Identify the preparation type.
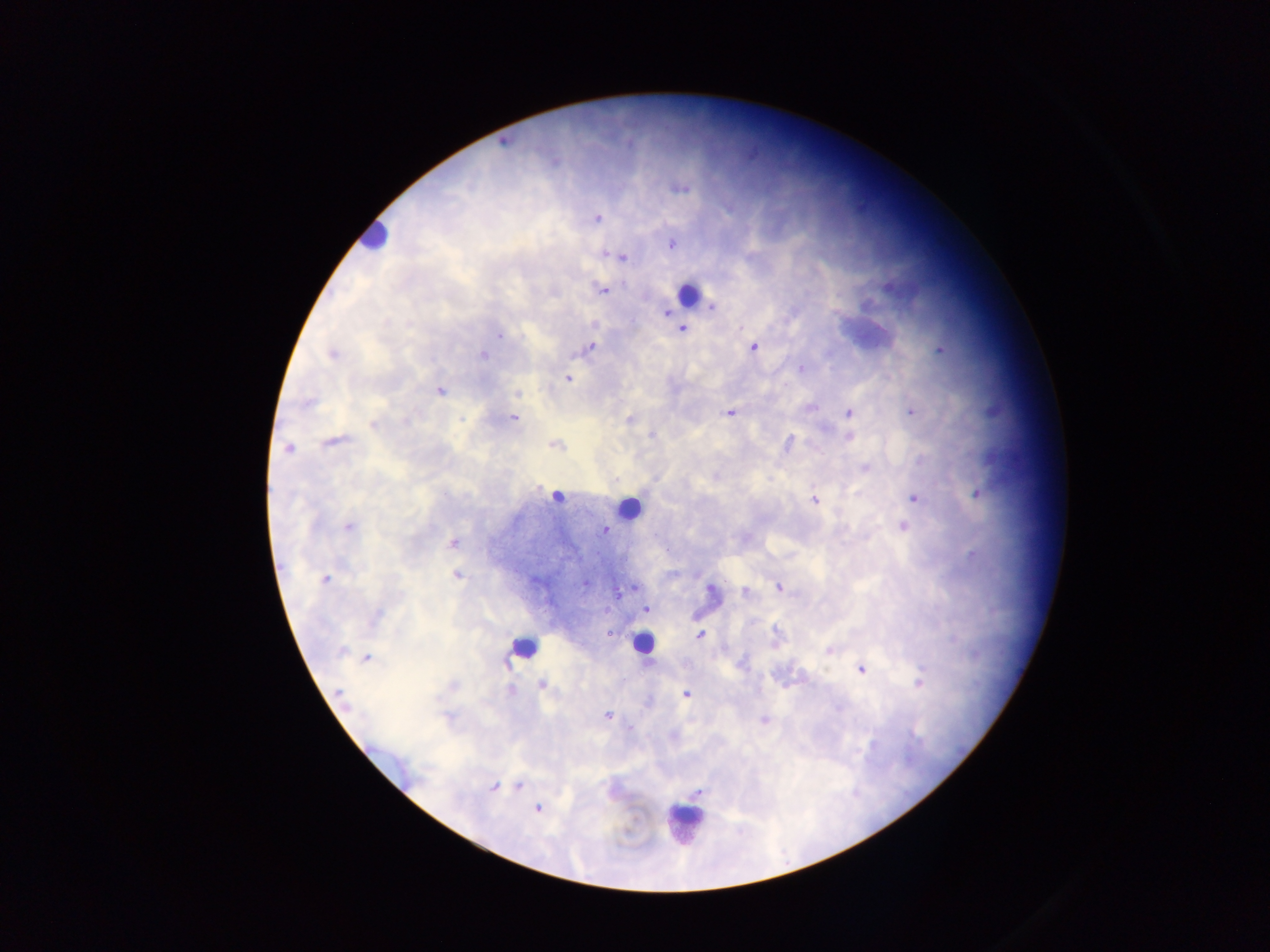

Thick blood film.

Approximate centers as [x, y] in pixels.
Summary:
  - Leukocyte locations: [374, 239], [687, 295], [626, 502], [526, 644], [649, 649], [694, 814]
  - Malaria parasite locations: [682, 187], [597, 218], [672, 244], [606, 252], [612, 254], [621, 257], [889, 284], [604, 290], [683, 328], [498, 335], [590, 346], [755, 347], [939, 351], [482, 355], [567, 377], [440, 391], [517, 393], [912, 411], [849, 412], [731, 414], [514, 419], [464, 420], [630, 420], [652, 435], [850, 437], [791, 441], [552, 445], [289, 448], [865, 468], [771, 479], [977, 492], [556, 496], [915, 498], [815, 500], [904, 525], [350, 526], [606, 529], [453, 544], [973, 554], [458, 576], [325, 580], [582, 584], [709, 586], [780, 588], [746, 591], [622, 592], [648, 609], [609, 634], [699, 635], [342, 649], [829, 650], [368, 658], [508, 662], [862, 669], [917, 680], [542, 684], [511, 689], [686, 694], [340, 696], [347, 707], [608, 715], [766, 721], [870, 743], [494, 787], [697, 793]
  - Capture: mobile-phone photograph through a microscope
  - Country: Ghana
  - Image size: 1270×952 pixels
  - Field of view: single